Assess the morphology of the red blood cells.
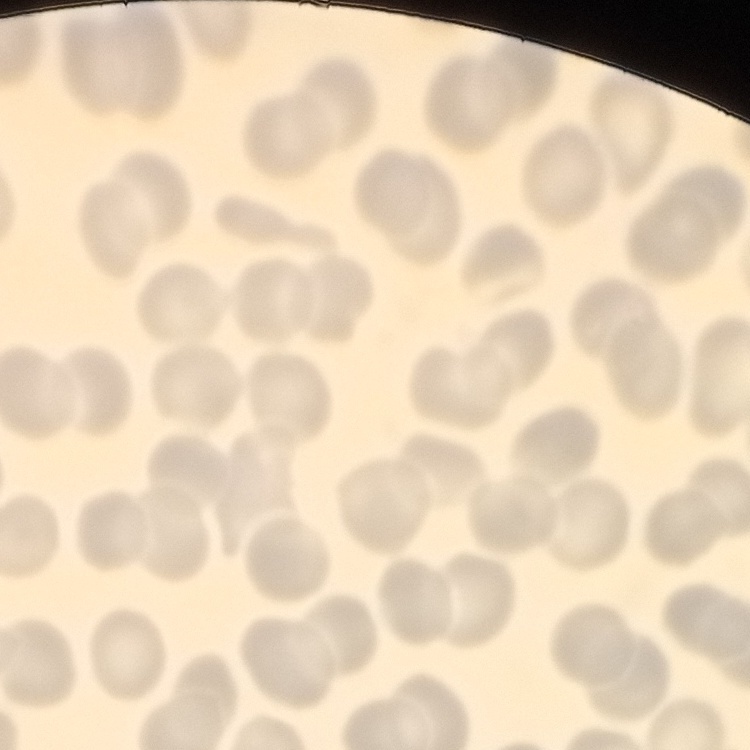

No rouleaux formation.

Stained with either Field's or Giemsa. Thin blood film. Square crop of a larger photomicrograph.